Report the malaria status of this cell.
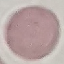
It is uninfected.

Giemsa stain. Cell patch, automatically extracted from a larger field of view and resized to 64 × 64 pixels. Photographed with a smartphone camera at the microscope eyepiece. Thin smear of blood.